Classify this cell by malaria status.
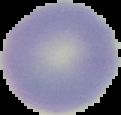
It is uninfected.

image type = segmented cell region on a black background
preparation = thin blood film
image size = 121×115 pixels